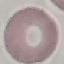
malaria_status: uninfected
image_type: automatically extracted cell patch, resized to 64 × 64 pixels
stain: Giemsa
capture: smartphone camera at the microscope eyepiece
preparation: thin blood film